Locate platelets.
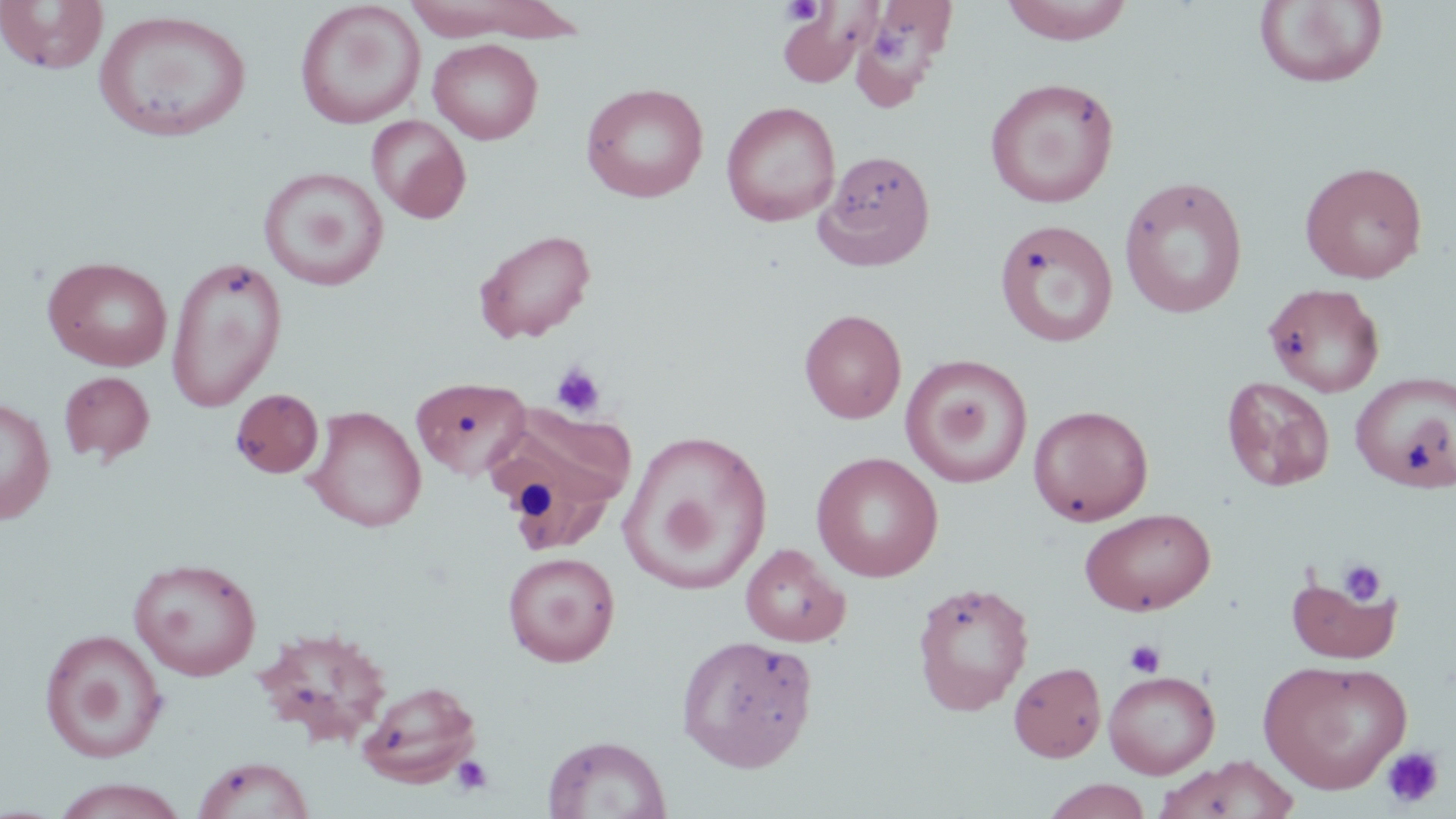

Approximate bounding boxes as named x1/y1/x2/y2 corners in pixels.
Platelets: (x1=781, y1=1, x2=824, y2=25), (x1=870, y1=23, x2=906, y2=62), (x1=550, y1=361, x2=607, y2=419), (x1=1337, y1=559, x2=1387, y2=607), (x1=1124, y1=640, x2=1166, y2=678), (x1=1380, y1=746, x2=1445, y2=809), (x1=451, y1=754, x2=494, y2=796).

Uninfected red blood cell locations: (x1=1000, y1=0, x2=1136, y2=45), (x1=0, y1=1, x2=109, y2=75), (x1=294, y1=1, x2=426, y2=129), (x1=398, y1=1, x2=578, y2=43), (x1=1253, y1=1, x2=1390, y2=90), (x1=859, y1=3, x2=956, y2=91), (x1=778, y1=6, x2=868, y2=87), (x1=93, y1=8, x2=252, y2=143), (x1=428, y1=38, x2=543, y2=144), (x1=984, y1=77, x2=1121, y2=208), (x1=581, y1=82, x2=709, y2=203), (x1=721, y1=100, x2=840, y2=227), (x1=367, y1=114, x2=471, y2=222), (x1=815, y1=149, x2=935, y2=270), (x1=1299, y1=160, x2=1428, y2=283), (x1=258, y1=166, x2=389, y2=291), (x1=1118, y1=175, x2=1249, y2=318), (x1=994, y1=219, x2=1119, y2=348), (x1=473, y1=229, x2=597, y2=344), (x1=43, y1=255, x2=173, y2=372), (x1=166, y1=256, x2=287, y2=411), (x1=1262, y1=282, x2=1386, y2=397), (x1=799, y1=308, x2=906, y2=424), (x1=901, y1=354, x2=1033, y2=489), (x1=58, y1=371, x2=155, y2=465), (x1=1350, y1=371, x2=1456, y2=493), (x1=1221, y1=375, x2=1336, y2=491), (x1=410, y1=376, x2=533, y2=481), (x1=230, y1=388, x2=324, y2=478), (x1=0, y1=397, x2=56, y2=524), (x1=486, y1=404, x2=637, y2=553), (x1=1028, y1=404, x2=1154, y2=525), (x1=304, y1=406, x2=427, y2=532), (x1=621, y1=430, x2=772, y2=595), (x1=811, y1=451, x2=944, y2=582), (x1=1079, y1=507, x2=1216, y2=616), (x1=741, y1=544, x2=851, y2=647), (x1=502, y1=551, x2=620, y2=667), (x1=128, y1=556, x2=262, y2=681), (x1=1286, y1=572, x2=1402, y2=665), (x1=912, y1=580, x2=1034, y2=716), (x1=253, y1=624, x2=395, y2=749), (x1=40, y1=629, x2=168, y2=764), (x1=677, y1=634, x2=818, y2=772), (x1=1258, y1=658, x2=1412, y2=794), (x1=1008, y1=661, x2=1106, y2=762), (x1=1103, y1=670, x2=1220, y2=779), (x1=357, y1=679, x2=482, y2=788), (x1=543, y1=734, x2=670, y2=819), (x1=1155, y1=755, x2=1303, y2=819), (x1=192, y1=756, x2=315, y2=818), (x1=50, y1=778, x2=191, y2=818), (x1=1040, y1=778, x2=1153, y2=818). Slide-level diagnosis: negative for blood parasites. 1000x magnification. One field of a larger specimen. Optical microscopy. May-Grünwald-Giemsa-stained preparation. Thin blood film. Image is 1456×819 pixels.